State the preparation type.
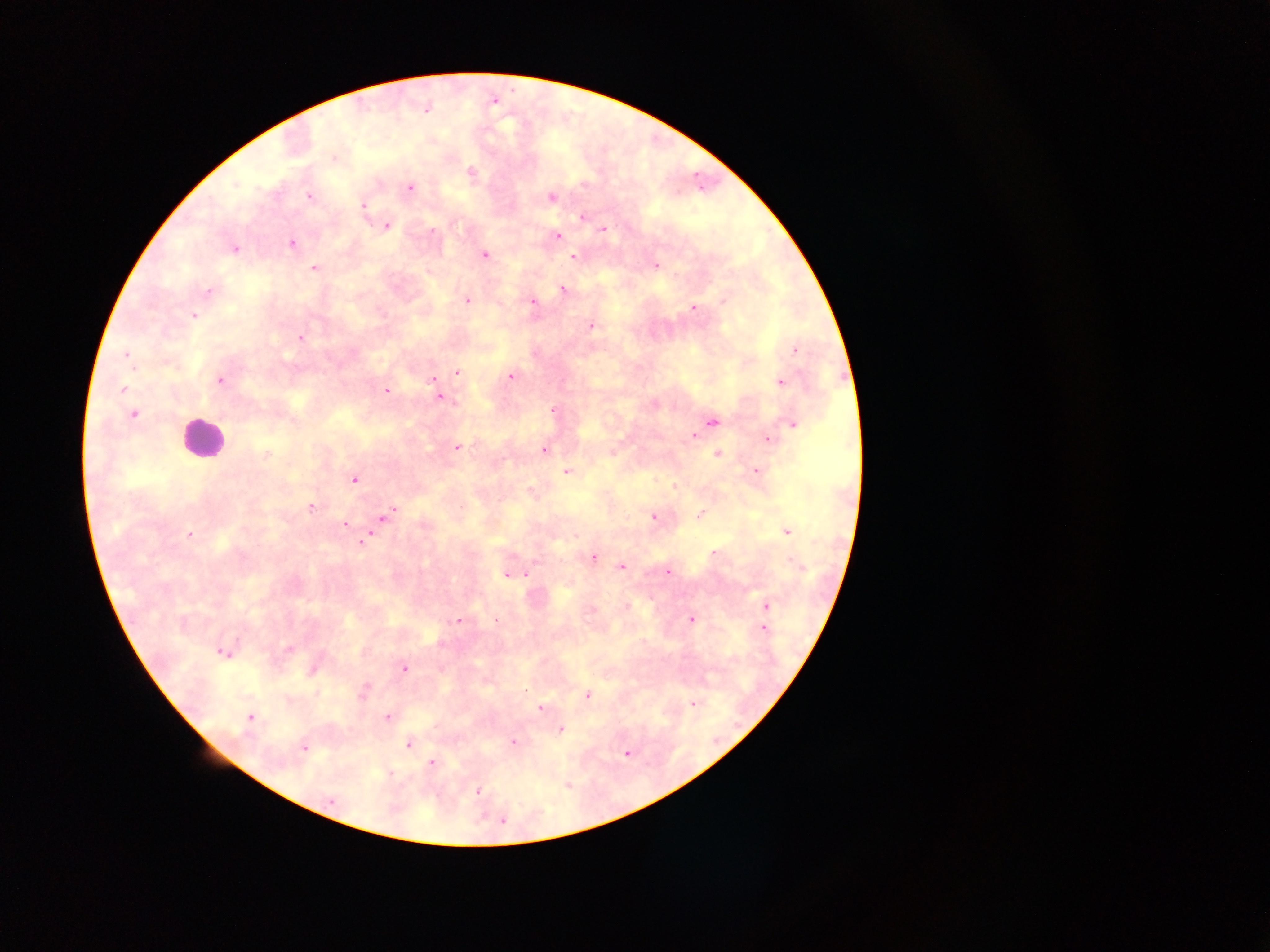
This is a thick smear.

Approximate centers as [x, y] in pixels. Plasmodium parasite locations: [425, 107], [334, 157], [471, 173], [409, 187], [308, 195], [551, 197], [363, 205], [582, 216], [386, 225], [602, 229], [557, 235], [291, 242], [233, 249], [484, 255], [573, 256], [654, 265], [314, 269], [562, 288], [208, 291], [466, 300], [533, 300], [693, 307], [193, 315], [590, 326], [299, 337], [795, 349], [126, 354], [457, 372], [511, 375], [433, 378], [219, 379], [780, 382], [437, 389], [123, 390], [386, 391], [439, 396], [552, 409], [132, 414], [711, 421], [792, 423], [703, 427], [694, 435], [767, 438], [457, 446], [543, 449], [612, 453], [717, 454], [265, 455], [755, 471], [566, 472], [354, 478], [674, 486], [310, 506], [391, 513], [699, 515], [383, 517], [654, 517], [345, 523], [787, 531], [189, 534], [363, 542], [592, 557], [620, 566], [668, 571], [506, 573], [524, 573], [766, 606], [624, 607], [591, 609], [691, 619], [458, 620], [763, 628], [288, 647], [222, 651], [314, 667], [403, 668], [364, 690], [587, 695], [694, 703], [541, 708], [249, 716], [386, 716], [559, 728], [512, 742], [408, 743], [303, 748], [626, 753], [432, 762], [567, 784], [477, 791], [330, 801], [501, 819]. Leukocyte locations: [201, 439]. Image is 1270×952 pixels. Collected in Ghana. One field of view. Mobile-phone photograph taken through the microscope.